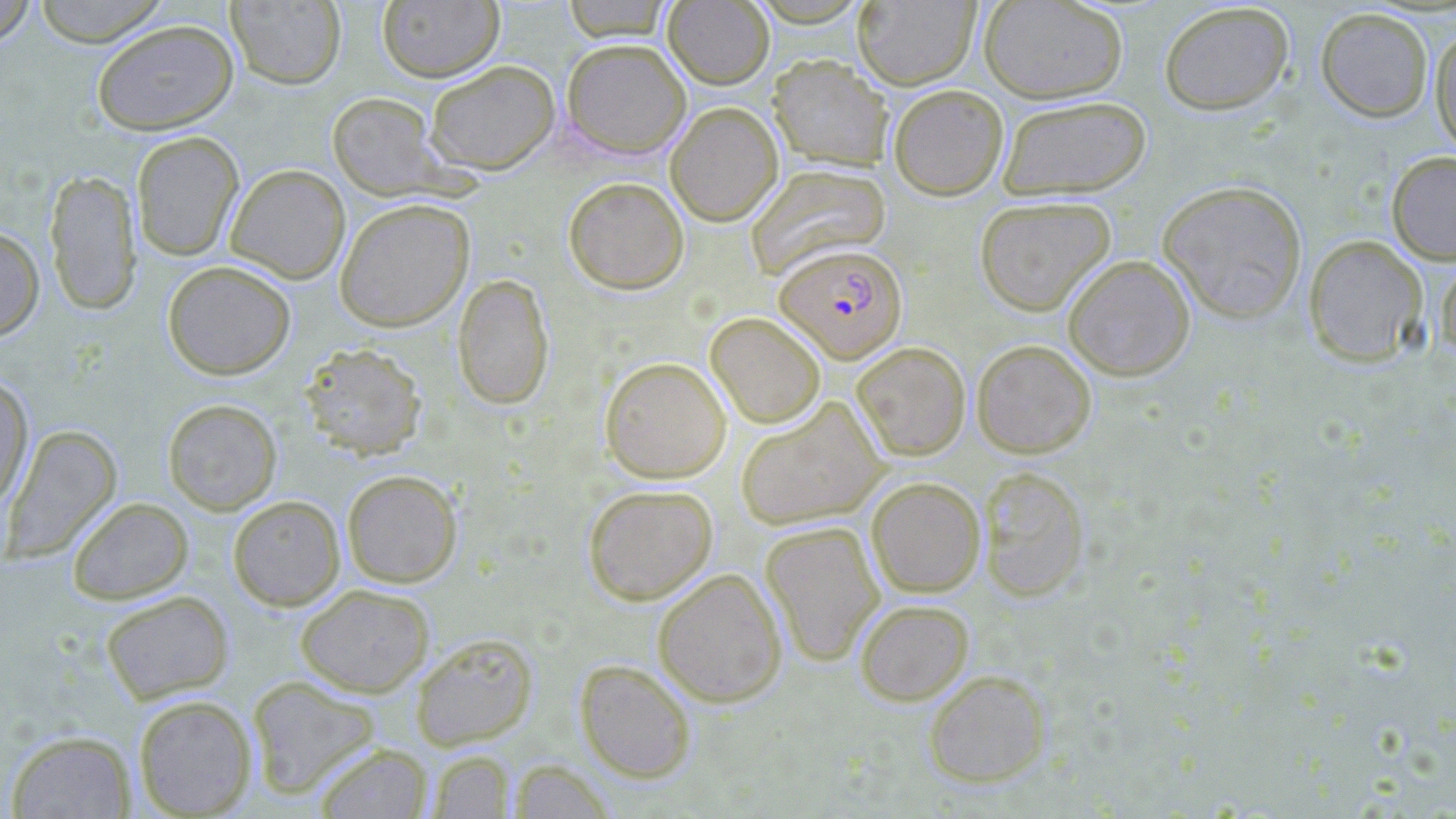

Approximate bounding boxes as [x1, y1, x2, y2] in pixels. Plasmodium falciparum-infected red blood cell locations: [774, 243, 908, 363]. Uninfected red blood cell locations: [32, 0, 171, 47], [561, 0, 675, 41], [979, 0, 1128, 103], [0, 1, 37, 50], [227, 1, 346, 89], [377, 1, 504, 83], [664, 1, 774, 89], [853, 1, 980, 90], [1158, 2, 1294, 115], [1316, 7, 1434, 122], [91, 19, 239, 135], [1430, 24, 1456, 156], [561, 38, 691, 159], [768, 55, 894, 171], [426, 60, 560, 175], [888, 84, 1008, 201], [327, 91, 446, 199], [997, 95, 1151, 201], [665, 101, 783, 226], [131, 131, 244, 261], [1386, 151, 1456, 265], [225, 163, 350, 284], [745, 164, 891, 277], [44, 168, 142, 316], [563, 176, 689, 294], [1157, 179, 1308, 323], [974, 196, 1116, 316], [334, 198, 475, 332], [0, 226, 44, 340], [1303, 234, 1429, 368], [1063, 254, 1195, 381], [1435, 254, 1456, 363], [162, 260, 296, 380], [452, 273, 555, 410], [706, 311, 826, 428], [972, 339, 1096, 458], [299, 342, 428, 460], [851, 342, 971, 460], [599, 356, 731, 483], [0, 373, 34, 512], [162, 398, 282, 515], [736, 398, 886, 529], [3, 424, 122, 562], [977, 466, 1090, 601], [342, 469, 463, 588], [866, 476, 985, 597], [583, 483, 718, 605], [228, 495, 346, 611], [67, 497, 193, 604], [760, 521, 885, 666], [652, 568, 787, 707], [296, 584, 434, 697], [100, 590, 234, 703], [854, 599, 974, 705], [411, 632, 539, 750], [575, 659, 697, 783], [923, 669, 1051, 788], [246, 675, 381, 799], [133, 694, 257, 817], [6, 730, 136, 818], [313, 742, 434, 819], [427, 750, 515, 818], [508, 759, 616, 819]. Slide-level diagnosis: Plasmodium falciparum. One field of a larger specimen. Image is 1456×819 pixels. Light microscopy. Thin blood smear. Captured at 1000x magnification. May-Grünwald-Giemsa stain.